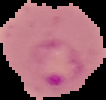

{
  "image_size": "106×100 pixels",
  "preparation": "thin blood film",
  "result": "Plasmodium parasites detected",
  "image_type": "segmented cell region with the area outside set to black"
}